Classify this cell by malaria status.
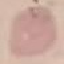

It is uninfected.

Thin blood smear. Giemsa stain. Photographed with a smartphone camera at the microscope eyepiece. Cell patch, automatically extracted from a larger field of view and resized to 64 × 64 pixels.